Give the extent of all Plasmodium ovale-infected red blood cells.
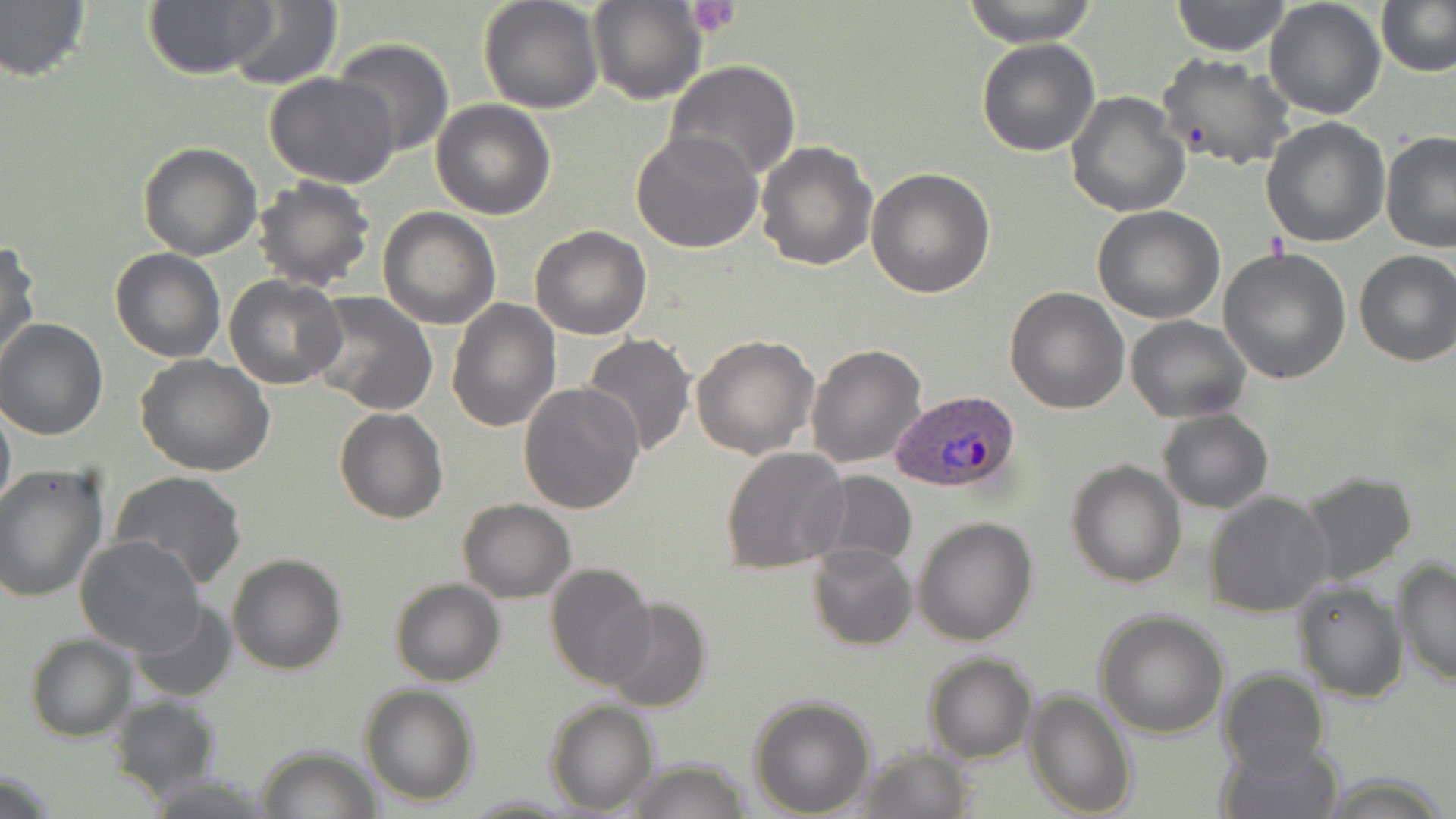
Approximate bounding boxes as named x1/y1/x2/y2 corners in pixels.
Plasmodium ovale-infected red blood cells: (x1=891, y1=389, x2=1022, y2=494).

slide_level_diagnosis: Plasmodium ovale
preparation: thin blood film
stain: May-Grünwald-Giemsa
platelet_locations: 'approximate bounding boxes as named x1/y1/x2/y2 corners in pixels: (x1=686, y1=0, x2=742, y2=36)'
modality: light microscopy
uninfected_red_blood_cell_locations: 'approximate bounding boxes as named x1/y1/x2/y2 corners in pixels: (x1=0, y1=0, x2=92, y2=87), (x1=222, y1=0, x2=343, y2=90), (x1=587, y1=0, x2=707, y2=104), (x1=959, y1=0, x2=1100, y2=47), (x1=1171, y1=0, x2=1292, y2=57), (x1=1264, y1=0, x2=1386, y2=120), (x1=1378, y1=0, x2=1454, y2=76), (x1=477, y1=1, x2=604, y2=114), (x1=143, y1=2, x2=273, y2=80), (x1=331, y1=37, x2=455, y2=157), (x1=976, y1=37, x2=1101, y2=158), (x1=1157, y1=53, x2=1296, y2=171), (x1=663, y1=60, x2=803, y2=184), (x1=265, y1=74, x2=402, y2=188), (x1=1066, y1=91, x2=1190, y2=217), (x1=431, y1=100, x2=556, y2=220), (x1=1260, y1=117, x2=1390, y2=248), (x1=629, y1=129, x2=764, y2=255), (x1=1380, y1=131, x2=1456, y2=253), (x1=754, y1=139, x2=878, y2=270), (x1=138, y1=142, x2=263, y2=259), (x1=866, y1=166, x2=996, y2=298), (x1=252, y1=176, x2=377, y2=292), (x1=377, y1=206, x2=502, y2=329), (x1=1092, y1=206, x2=1225, y2=325), (x1=530, y1=225, x2=651, y2=340), (x1=0, y1=238, x2=40, y2=369), (x1=1218, y1=246, x2=1351, y2=384), (x1=110, y1=248, x2=227, y2=362), (x1=1353, y1=249, x2=1456, y2=366), (x1=224, y1=275, x2=346, y2=390), (x1=1004, y1=286, x2=1130, y2=413), (x1=307, y1=294, x2=438, y2=415), (x1=446, y1=298, x2=561, y2=433), (x1=1125, y1=315, x2=1251, y2=422), (x1=0, y1=319, x2=109, y2=439), (x1=580, y1=334, x2=695, y2=456), (x1=691, y1=335, x2=820, y2=459), (x1=806, y1=343, x2=926, y2=468), (x1=136, y1=355, x2=277, y2=477), (x1=517, y1=381, x2=644, y2=516), (x1=0, y1=397, x2=14, y2=522), (x1=334, y1=408, x2=448, y2=525), (x1=1156, y1=408, x2=1274, y2=512), (x1=721, y1=444, x2=850, y2=575), (x1=1066, y1=460, x2=1186, y2=587), (x1=0, y1=463, x2=108, y2=603), (x1=109, y1=471, x2=247, y2=589), (x1=1297, y1=471, x2=1418, y2=587), (x1=812, y1=472, x2=916, y2=569), (x1=1203, y1=491, x2=1334, y2=618), (x1=457, y1=499, x2=576, y2=602), (x1=913, y1=518, x2=1039, y2=646), (x1=74, y1=535, x2=207, y2=658), (x1=807, y1=542, x2=917, y2=651), (x1=226, y1=554, x2=347, y2=675), (x1=1393, y1=560, x2=1455, y2=687), (x1=545, y1=564, x2=658, y2=689), (x1=389, y1=577, x2=505, y2=687), (x1=1293, y1=578, x2=1409, y2=702), (x1=132, y1=599, x2=238, y2=703), (x1=603, y1=599, x2=713, y2=714), (x1=1094, y1=610, x2=1230, y2=738), (x1=26, y1=636, x2=135, y2=741), (x1=924, y1=652, x2=1035, y2=763), (x1=1218, y1=668, x2=1330, y2=779), (x1=360, y1=682, x2=480, y2=805), (x1=1024, y1=688, x2=1137, y2=815), (x1=748, y1=693, x2=877, y2=815), (x1=107, y1=696, x2=222, y2=801), (x1=545, y1=700, x2=659, y2=815), (x1=1215, y1=739, x2=1343, y2=819), (x1=256, y1=744, x2=381, y2=818), (x1=850, y1=745, x2=975, y2=818), (x1=620, y1=757, x2=754, y2=818), (x1=462, y1=794, x2=578, y2=816)'
image_size: 1456×819 pixels
magnification: 1000x
field_of_view: one of a larger specimen